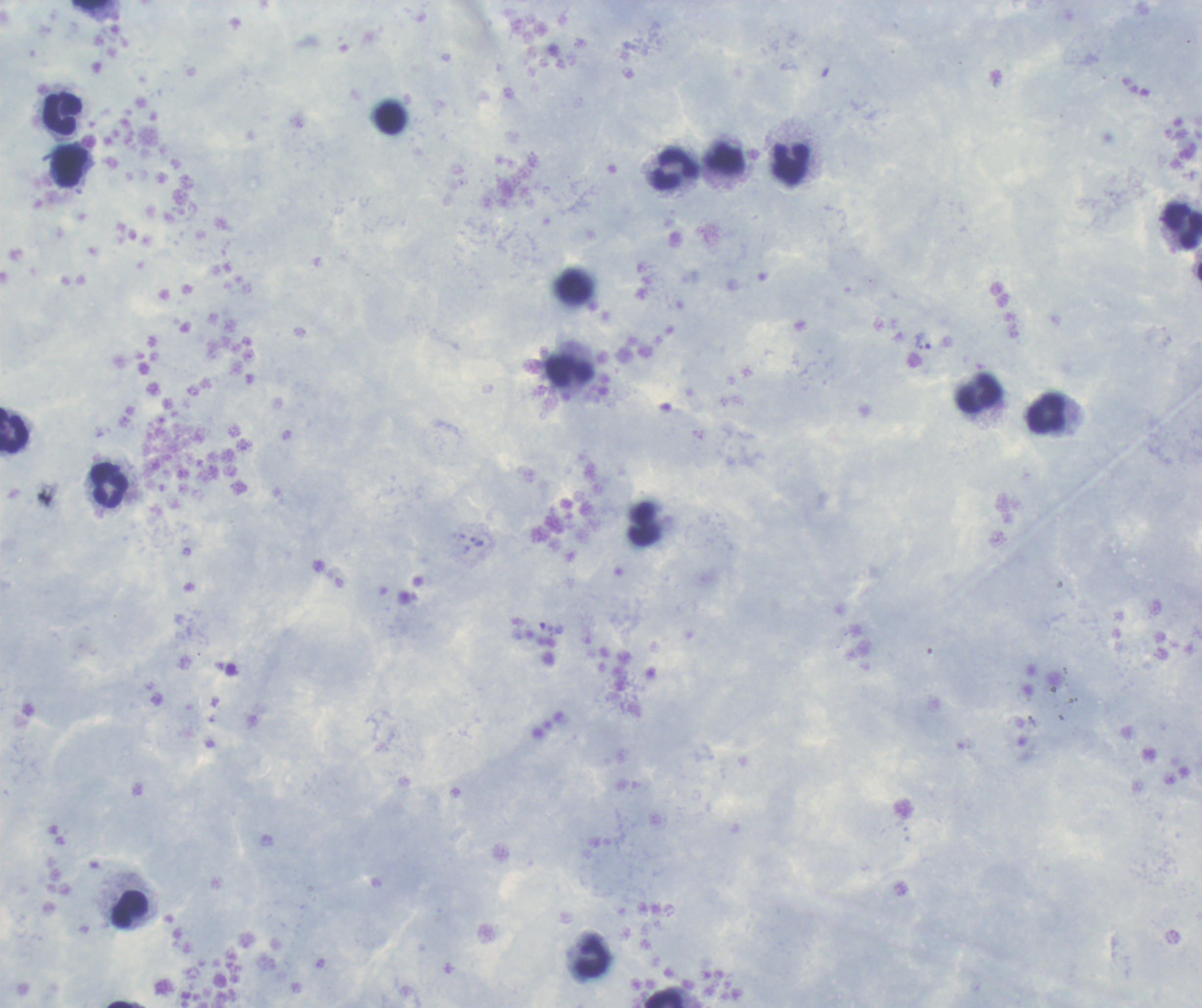
{
  "field_of_view": "single",
  "magnification": "100x",
  "context": "previously used in an actual diagnosis",
  "coloration_quality": "good",
  "preparation": "thick blood film",
  "background_quality": "satisfactory",
  "image_size": "1202×1008 pixels",
  "trophozoite_locations": "approximate centers as (x, y) in pixels: (923, 341), (476, 541), (546, 627)",
  "stain": "Romanowsky",
  "leukocyte_locations": "approximate centers as (x, y) in pixels: (63, 114), (392, 118), (791, 164), (70, 167), (675, 171), (1183, 225), (570, 371), (979, 393), (1046, 413), (14, 431), (110, 486), (642, 523), (130, 909), (593, 957), (664, 999)",
  "result": "malaria parasites detected"
}